Describe the morphology of the red blood cells.
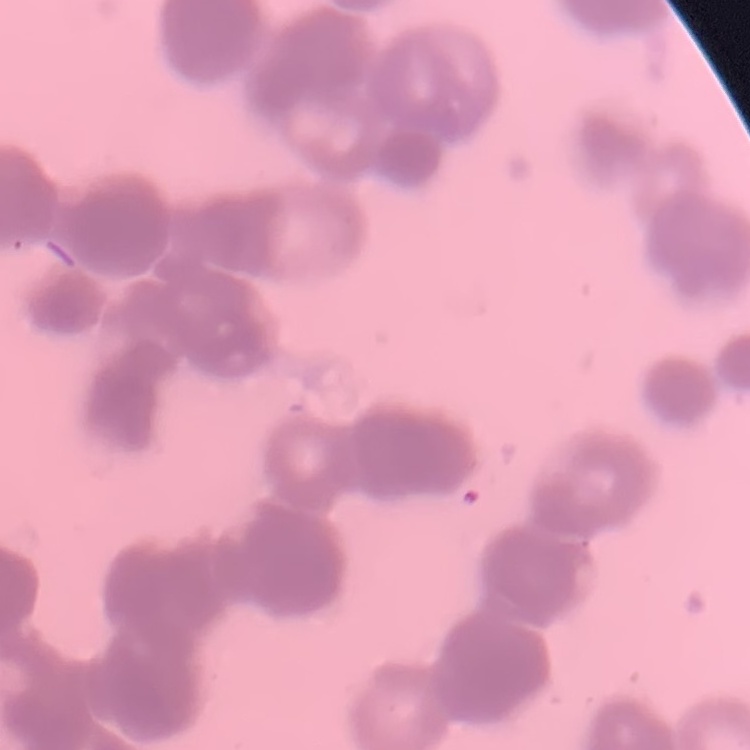
They show rouleaux formation.

Stained with either Field's or Giemsa. Thin peripheral smear. One tile cut from a larger photomicrograph.